Identify the parasite.
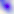
This is Toxoplasma gondii.

Summary:
  - Magnification: 400x
  - Modality: micrograph